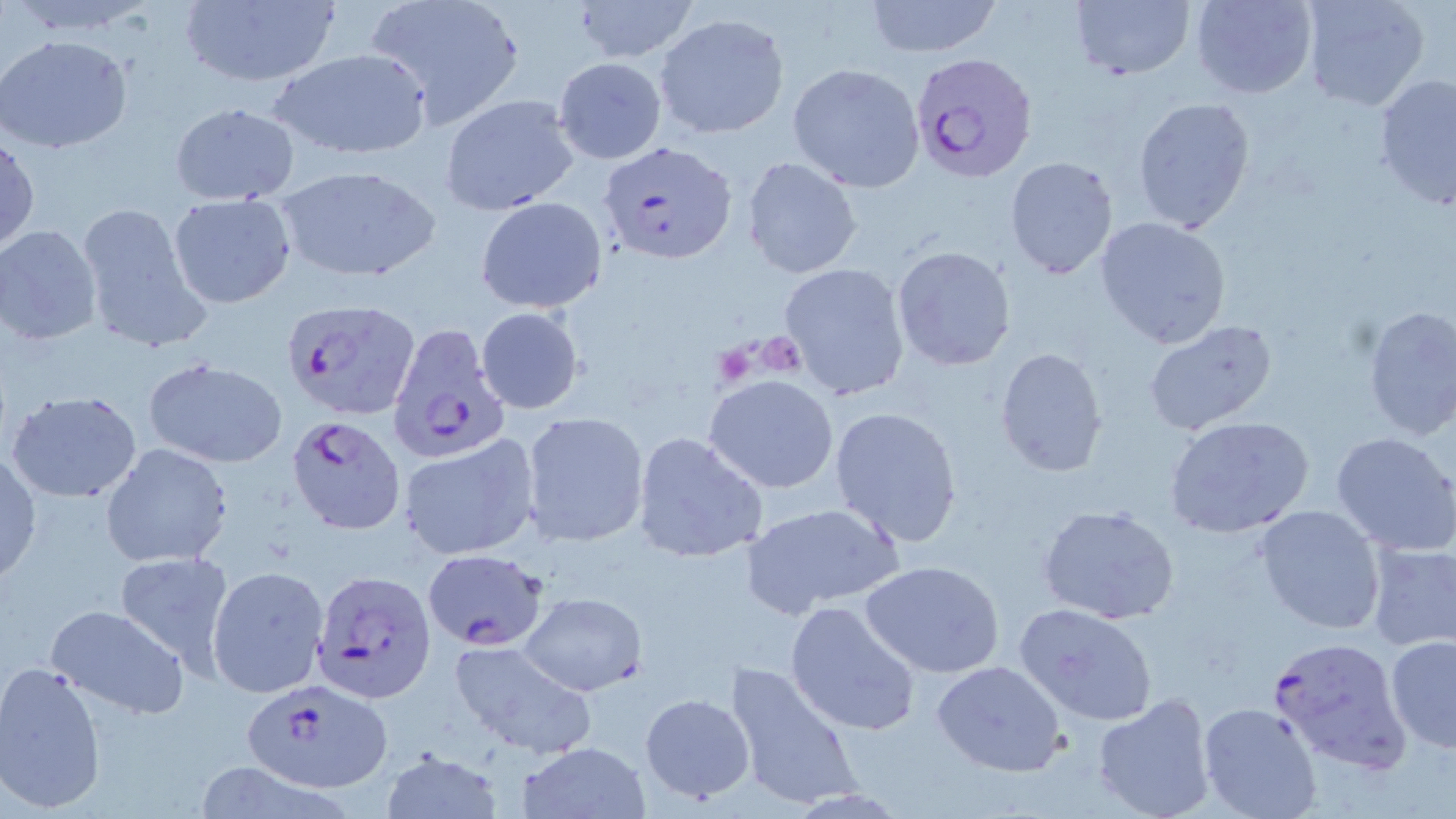
slide-level diagnosis = Plasmodium falciparum
field of view = one of a larger specimen
modality = light microscopy
preparation = thin blood film
magnification = 1000x
Plasmodium falciparum-infected red blood cell locations = approximate bounding boxes as (x1,y1)-(x2,y2) corner pairs in pixels: (913,53)-(1039,185), (598,138)-(735,266), (281,296)-(419,421), (393,326)-(500,472), (287,414)-(406,535), (423,547)-(551,651), (309,569)-(434,703), (1267,635)-(1413,772), (240,679)-(394,792)
uninfected red blood cell locations = approximate bounding boxes as (x1,y1)-(x2,y2) corner pairs in pixels: (362,0)-(525,128), (572,0)-(701,63), (864,0)-(1005,57), (1069,0)-(1198,81), (1192,0)-(1317,99), (1302,0)-(1433,111), (174,1)-(342,89), (653,13)-(790,138), (1,34)-(132,154), (270,48)-(433,161), (553,57)-(667,165), (787,62)-(925,193), (1373,73)-(1456,211), (440,93)-(580,215), (1130,97)-(1254,233), (169,103)-(300,205), (1,134)-(39,255), (1003,156)-(1120,279), (742,157)-(863,279), (273,164)-(440,284), (167,193)-(295,308), (475,196)-(608,315), (75,198)-(213,353), (1094,216)-(1233,350), (0,225)-(105,346), (892,245)-(1016,371), (777,262)-(911,401), (1359,304)-(1456,441), (475,306)-(584,415), (1140,319)-(1281,437), (994,346)-(1109,479), (141,356)-(289,468), (705,375)-(840,493), (8,390)-(144,503), (828,406)-(965,547), (521,411)-(650,546), (1163,414)-(1316,541), (1329,430)-(1456,556), (632,431)-(769,563), (397,434)-(541,562), (101,444)-(234,567), (0,450)-(42,584), (740,501)-(905,616), (1038,502)-(1181,626), (1255,507)-(1386,633), (1366,542)-(1456,654), (112,549)-(239,678), (862,562)-(1005,678), (207,565)-(329,697), (519,592)-(646,696), (786,599)-(922,736), (1013,602)-(1159,725), (43,604)-(191,721), (1385,636)-(1456,752), (448,639)-(597,757), (933,659)-(1067,778), (0,660)-(107,813), (724,660)-(862,812), (638,692)-(757,803), (1091,694)-(1218,819), (1199,703)-(1322,819), (517,740)-(652,819), (376,748)-(508,819), (190,761)-(358,819)
platelet locations = approximate bounding boxes as (x1,y1)-(x2,y2) corner pairs in pixels: (760,336)-(812,385), (711,344)-(757,389)
stain = May-Grünwald-Giemsa
image size = 1456×819 pixels